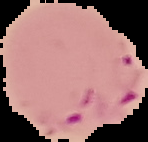 Segmented cell region on a black background. From a thin blood smear. Result: malaria parasites detected. Image is 148×142 pixels.